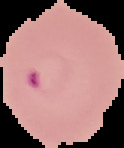
Segmented cell region on a black background. From a thin blood film. Result: Plasmodium parasites identified. Image is 124×148 pixels.